Give the position of every Plasmodium parasite visible.
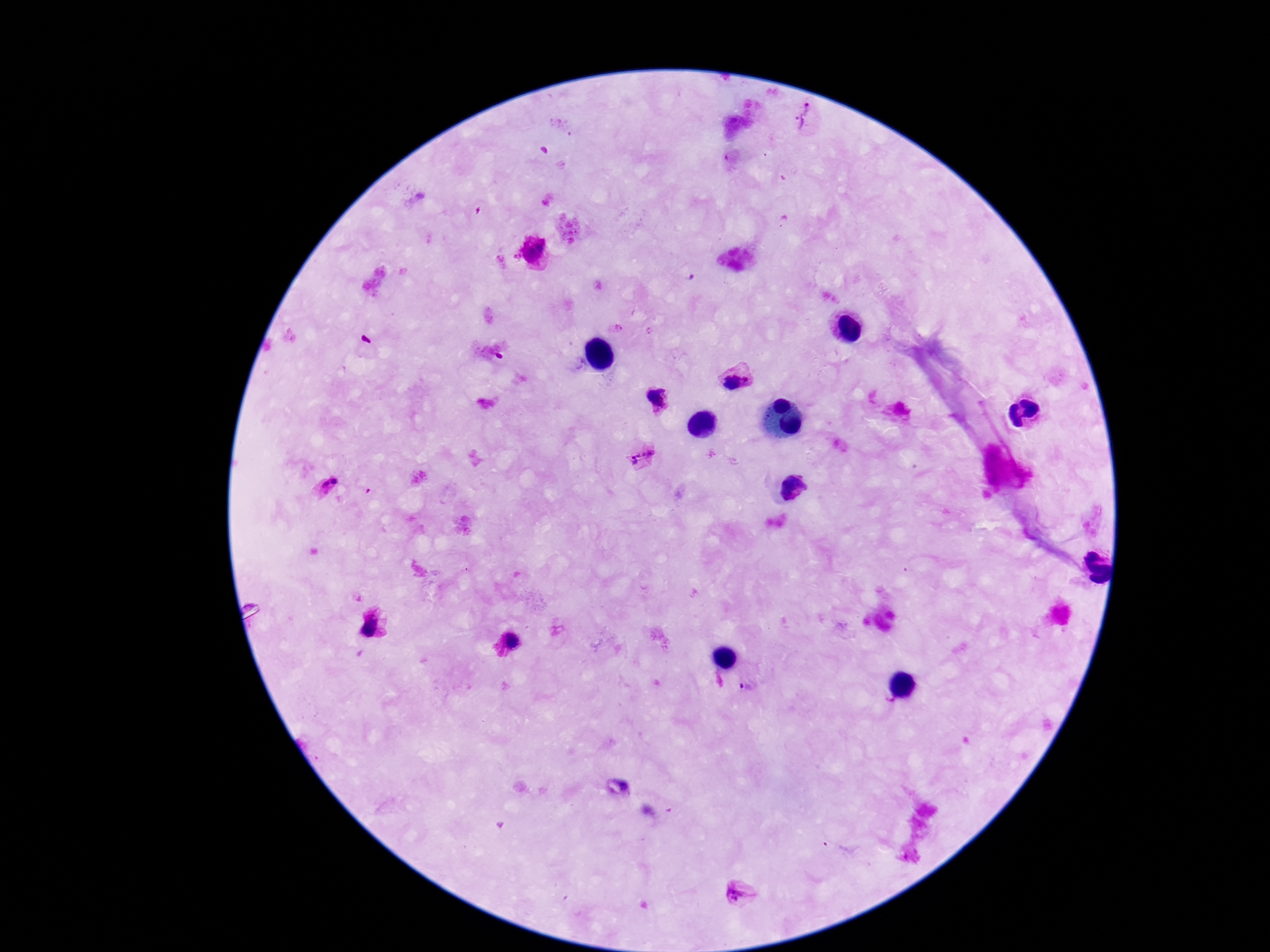

Approximate centers as (x, y) in pixels.
Plasmodium parasites: (806, 116), (541, 247), (529, 253), (737, 380), (657, 398), (642, 458), (335, 481), (325, 484), (792, 488), (374, 627), (513, 639), (747, 688), (742, 895).

Patient malaria status: infected. Smartphone photograph taken through the microscope eyepiece. 100x magnification. Image is 1270×952 pixels. One field from this slide. Thick peripheral-blood smear. Giemsa stain.